State which parasite is depicted.
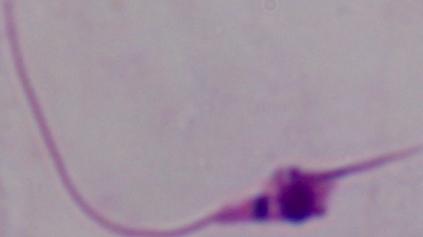
This is Leishmania.

1000x magnification. Micrograph.